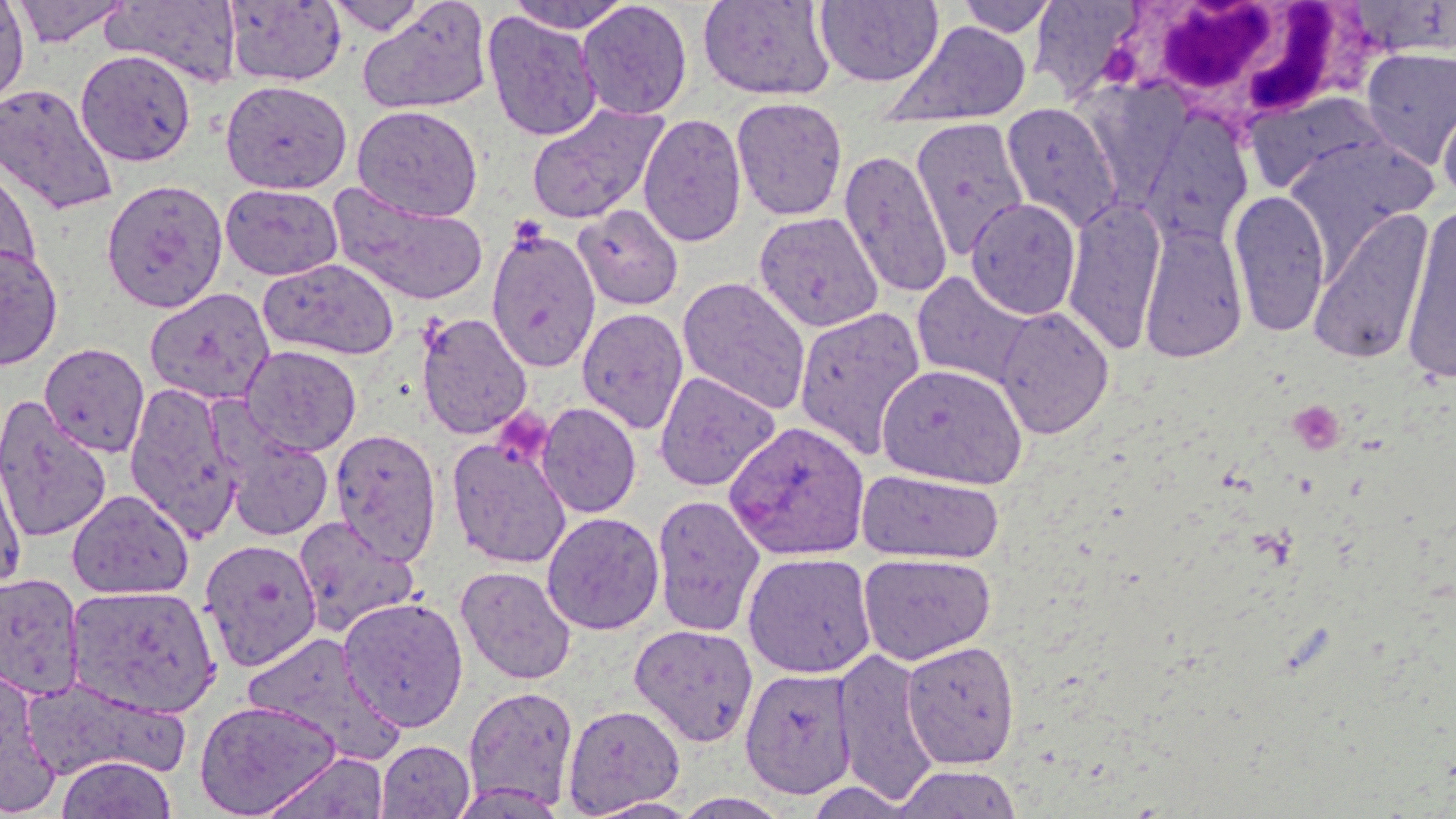

slide-level diagnosis = Plasmodium ovale
stain = May-Grünwald-Giemsa
platelet locations = approximate bounding boxes as [x1, y1, x2, y2] in pixels: [1291, 406, 1340, 463], [499, 410, 558, 465]
preparation = thin blood film
magnification = 1000x
field of view = single
white blood cell locations = approximate bounding boxes as [x1, y1, x2, y2] in pixels: [1118, 1, 1363, 138]
Plasmodium ovale-infected red blood cell locations = approximate bounding boxes as [x1, y1, x2, y2] in pixels: [724, 420, 870, 561]
uninfected red blood cell locations = approximate bounding boxes as [x1, y1, x2, y2] in pixels: [0, 0, 30, 110], [10, 0, 131, 47], [223, 0, 347, 87], [323, 0, 431, 35], [505, 0, 637, 33], [576, 0, 693, 120], [698, 0, 836, 101], [814, 0, 944, 87], [950, 0, 1063, 38], [103, 1, 243, 87], [1027, 1, 1145, 98], [357, 2, 493, 115], [481, 11, 603, 142], [880, 20, 1032, 130], [1358, 45, 1456, 170], [75, 49, 196, 167], [220, 79, 353, 195], [0, 83, 119, 217], [1246, 90, 1400, 196], [1436, 94, 1456, 206], [731, 96, 849, 221], [1000, 101, 1122, 233], [525, 102, 669, 226], [352, 105, 483, 222], [637, 113, 747, 248], [1138, 115, 1254, 250], [910, 117, 1030, 261], [1283, 134, 1439, 257], [839, 148, 953, 300], [0, 163, 42, 288], [101, 178, 229, 314], [219, 183, 344, 281], [327, 184, 490, 307], [1228, 189, 1332, 337], [1062, 194, 1167, 357], [967, 198, 1081, 320], [1400, 202, 1456, 384], [572, 204, 685, 310], [1308, 207, 1435, 366], [753, 211, 885, 333], [1139, 220, 1248, 363], [485, 227, 601, 374], [0, 243, 64, 371], [258, 257, 400, 361], [911, 271, 1036, 389], [677, 275, 812, 415], [144, 287, 276, 406], [995, 306, 1114, 439], [577, 307, 689, 434], [794, 307, 926, 460], [416, 312, 534, 439], [39, 342, 150, 458], [240, 345, 363, 456], [877, 362, 1028, 489], [652, 370, 780, 492], [124, 381, 243, 541], [0, 396, 114, 543], [536, 402, 642, 519], [329, 428, 442, 564], [220, 429, 334, 541], [446, 436, 572, 569], [0, 447, 28, 593], [856, 468, 1005, 565], [66, 489, 194, 599], [651, 493, 766, 637], [541, 511, 664, 635], [292, 516, 421, 637], [198, 538, 323, 670], [742, 551, 877, 679], [858, 552, 996, 665], [455, 565, 578, 685], [0, 571, 86, 702], [66, 584, 223, 718], [337, 595, 470, 732], [628, 622, 758, 746], [240, 632, 402, 761], [902, 639, 1020, 767], [833, 646, 940, 806], [0, 663, 58, 814], [740, 666, 855, 799], [21, 677, 188, 783], [463, 685, 579, 811], [193, 698, 343, 817], [563, 703, 685, 816], [375, 739, 475, 818], [55, 755, 178, 819], [891, 764, 1025, 819]
image size = 1456×819 pixels
modality = light microscopy